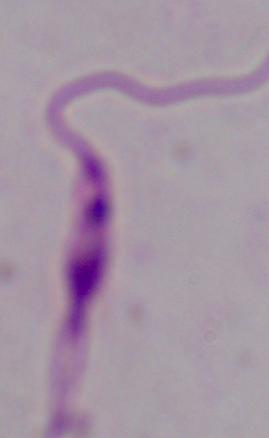

Summary:
  - Magnification: 1000x
  - Modality: photomicrograph
  - Identification: Leishmania